Give a bounding box for every parasitised red blood cell.
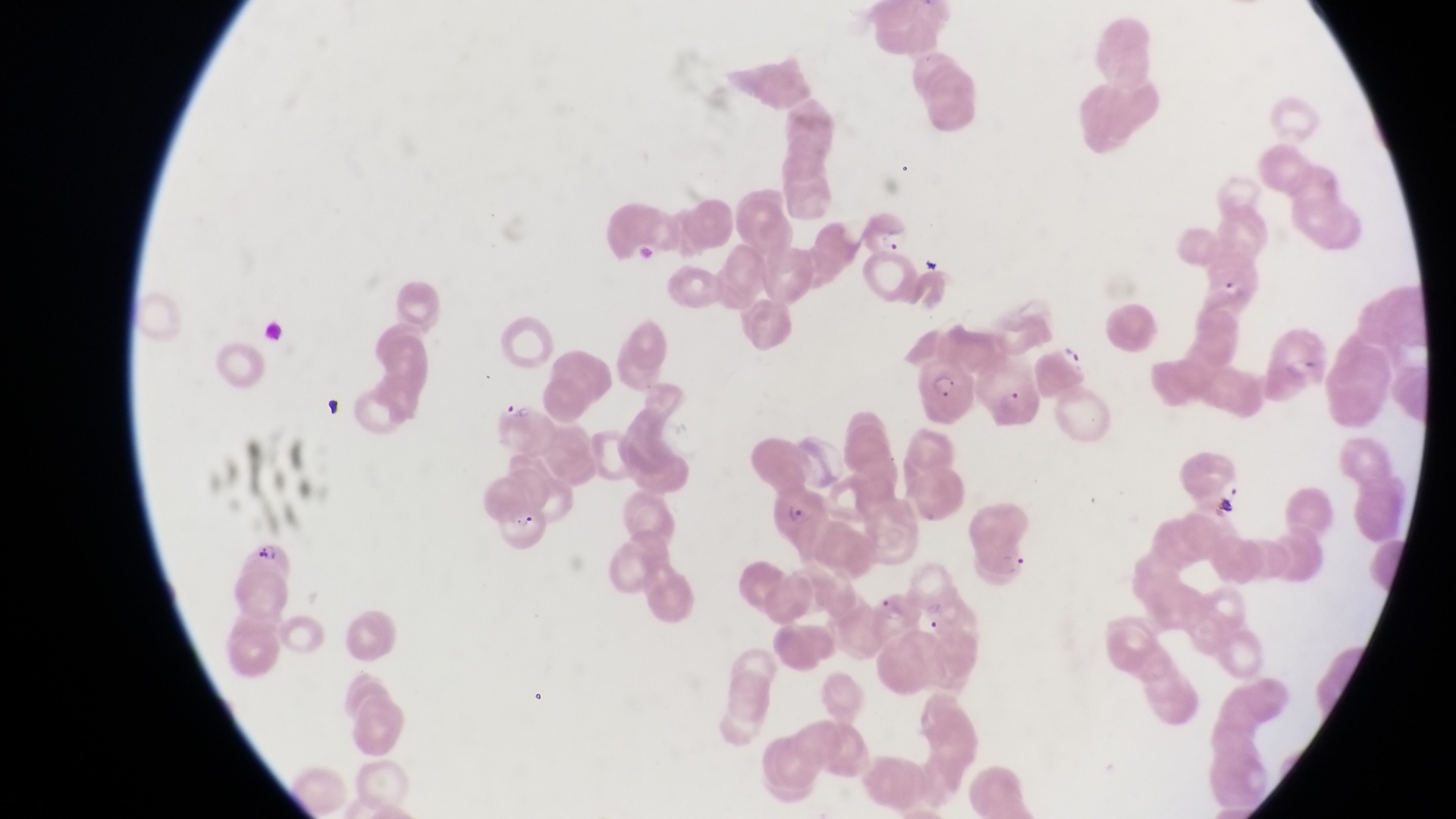

Approximate bounding boxes as {left, top, right, bottom} in pixels.
Parasitised red blood cells: {1269, 325, 1333, 398}, {925, 353, 980, 429}, {770, 482, 830, 540}, {240, 541, 290, 627}.

capture = smartphone photograph through the eyepiece of an Olympus CX-23 microscope
country = Uganda
image size = 1456×819 pixels
trophozoite locations = approximate bounding boxes as {left, top, right, bottom} in pixels: {878, 227, 910, 254}, {1062, 341, 1089, 371}
magnification = 1000x
artifact (platelet-like body, stain precipitate, or debris) locations = approximate bounding boxes as {left, top, right, bottom} in pixels: {914, 248, 947, 282}, {320, 396, 352, 422}, {508, 402, 532, 425}, {1213, 495, 1243, 525}, {515, 510, 536, 534}
preparation = thin blood smear
field of view = single